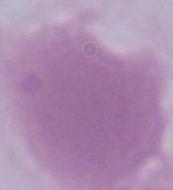
An erythrocyte is shown. Micrograph. 1000x magnification.